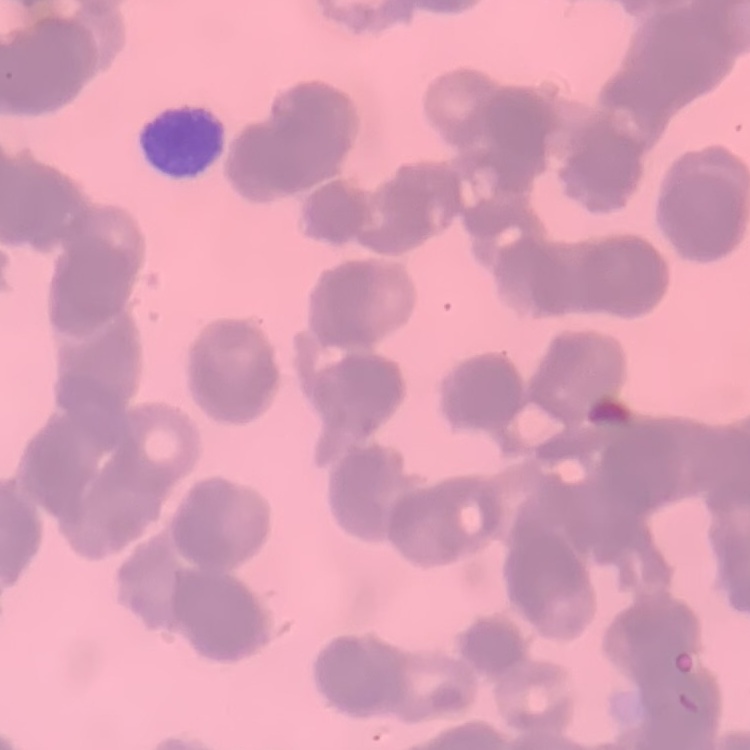

Summary:
  - Erythrocyte morphology: rouleaux formation
  - Stain: Field's or Giemsa
  - Image type: one tile cut from a larger photomicrograph
  - Preparation: thin blood smear